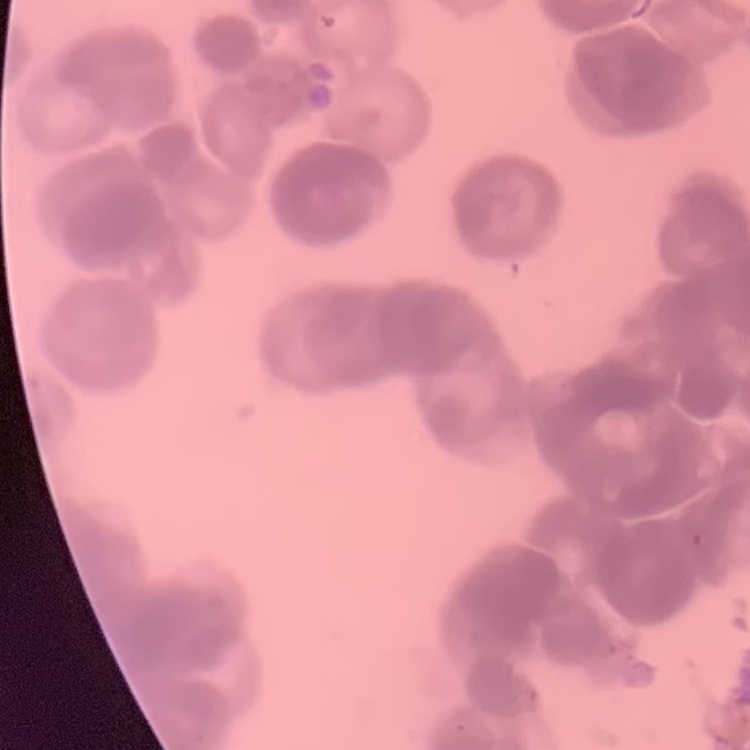

red blood cell morphology = rouleaux formation
stain = Field's or Giemsa
preparation = thin peripheral smear
image type = one tile cut from a larger photomicrograph